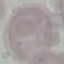

malaria_status: uninfected
stain: Giemsa
capture: smartphone through the microscope eyepiece
preparation: thin smear
image_type: cell patch, automatically extracted from a larger field of view and resized to 64 × 64 pixels